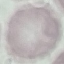 Result: negative for malaria parasites. Giemsa-stained preparation. Acquired by smartphone through the microscope eyepiece. Cell patch, automatically extracted from a larger field of view and resized to 64 × 64 pixels. Thin smear of blood.